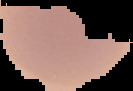

Summary:
  - Preparation: thin blood smear
  - Malaria status: uninfected
  - Image type: cell region segmented out of the field of view; surrounding area masked to black
  - Image size: 133×91 pixels